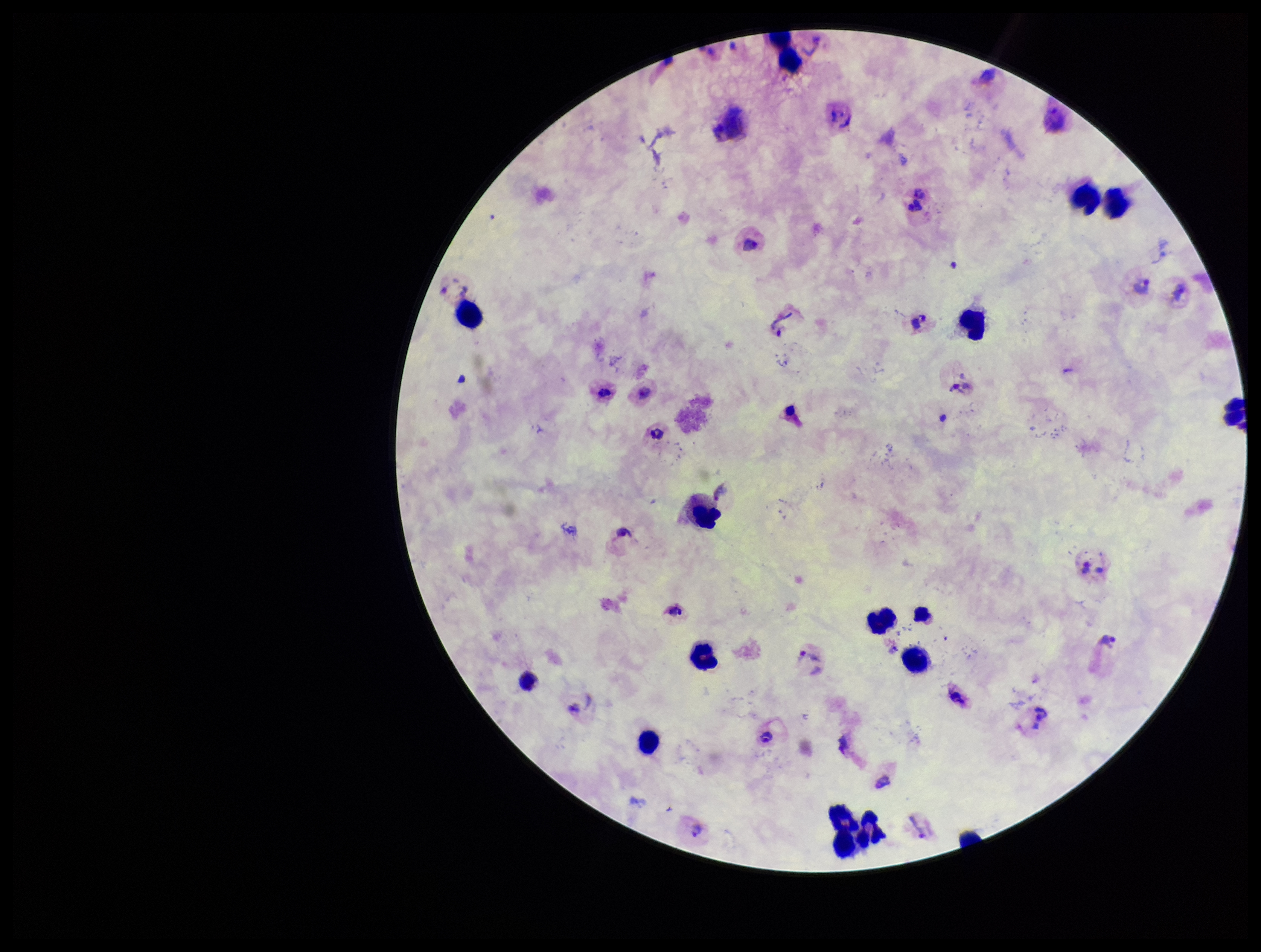
{
  "patient_malaria_status": "positive",
  "plasmodium_parasites": "detected",
  "parasite_count": 6,
  "image_size": "1261×952 pixels",
  "field_of_view": "single",
  "capture": "smartphone photograph through the microscope eyepiece",
  "species_reported_for_this_patient": "Plasmodium vivax",
  "stain": "Giemsa",
  "preparation": "thick blood smear",
  "leukocyte_count": 14
}